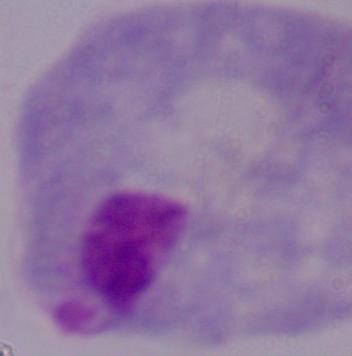

Summary:
  - Modality: micrograph
  - Identification: trichomonad
  - Magnification: 1000x